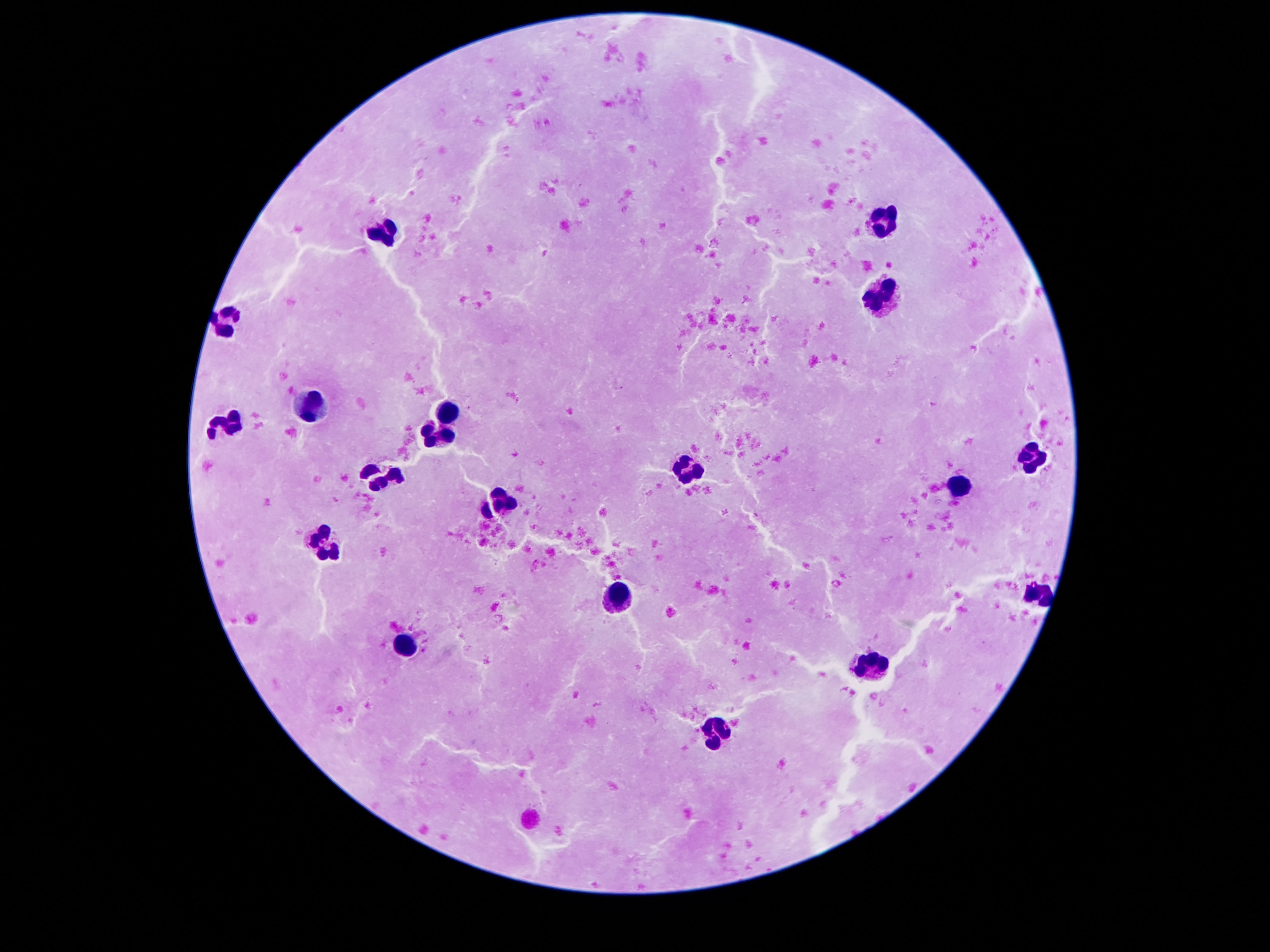
image_size: 1270×952 pixels
field_of_view: single
capture: smartphone camera through the microscope eyepiece
magnification: 100x
stain: Giemsa
patient_malaria_status: negative
leukocyte_locations: 'approximate centers as {x, y} in pixels: {888, 221}, {384, 230}, {883, 298}, {228, 321}, {312, 405}, {448, 413}, {232, 423}, {432, 437}, {1027, 459}, {686, 468}, {380, 479}, {958, 488}, {504, 500}, {327, 547}, {1038, 592}, {623, 596}, {407, 643}, {874, 668}, {716, 733}'
preparation: thick peripheral-blood smear